Outline each white blood cell.
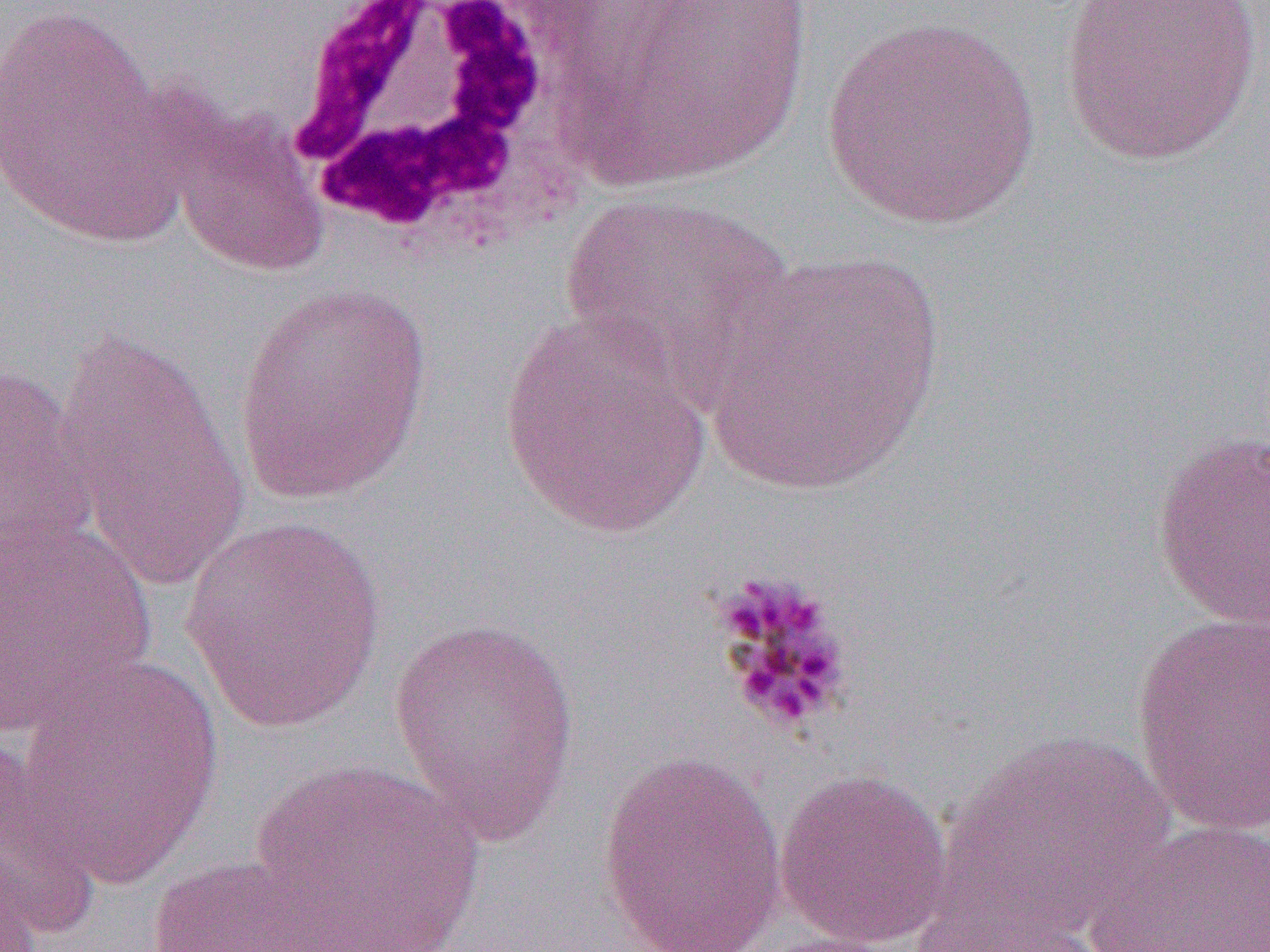

Approximate bounding boxes as [x1, y1, x2, y2] in pixels.
White blood cells: [266, 0, 602, 266].

Platelet locations: [708, 569, 856, 736]. Uninfected red blood cell locations: [569, 0, 815, 186], [1055, 0, 1265, 167], [0, 2, 175, 241], [820, 17, 1043, 230], [166, 106, 327, 277], [560, 191, 795, 388], [702, 250, 945, 497], [233, 281, 433, 504], [499, 313, 713, 538], [50, 331, 251, 590], [0, 363, 97, 563], [1151, 430, 1270, 630], [0, 514, 157, 737], [179, 514, 386, 733], [1130, 613, 1269, 838], [390, 616, 581, 844], [13, 653, 226, 887], [938, 729, 1174, 937], [0, 739, 105, 940], [595, 749, 789, 951], [249, 758, 488, 948], [774, 768, 953, 950], [1089, 818, 1270, 952], [0, 844, 45, 952], [142, 854, 351, 952], [910, 881, 1106, 952], [748, 932, 915, 952]. Slide-level diagnosis: Plasmodium malariae. Optical microscopy. One field of a larger specimen. Image is 1270×952 pixels. Thin blood film. 1000x magnification.